Locate platelets.
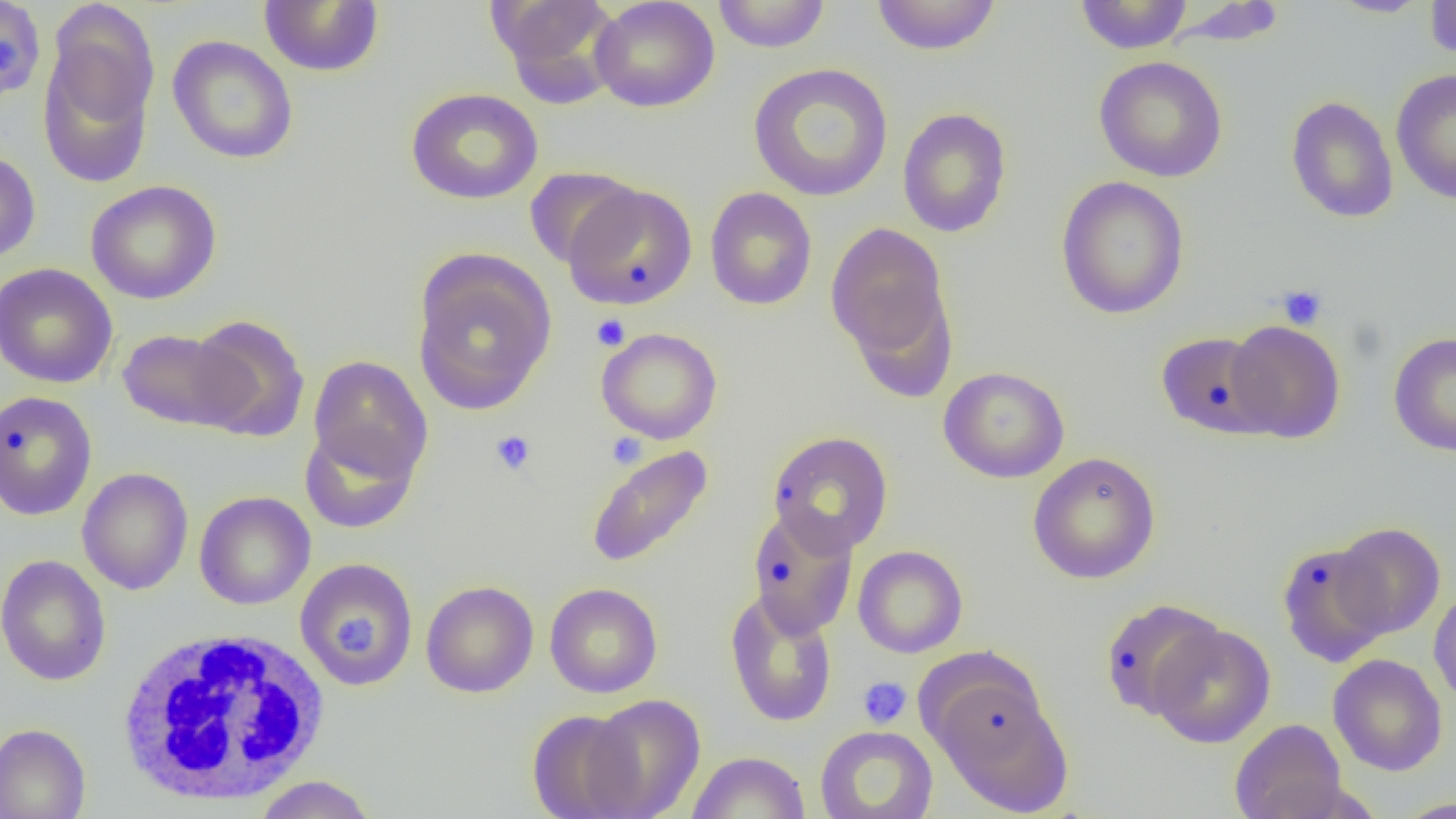

Approximate bounding boxes as named x1/y1/x2/y2 corners in pixels.
Platelets: (x1=1276, y1=284, x2=1328, y2=329), (x1=591, y1=313, x2=631, y2=350), (x1=490, y1=430, x2=536, y2=476), (x1=606, y1=433, x2=647, y2=469), (x1=858, y1=676, x2=912, y2=729).

Summary:
  - White blood cell locations: (x1=114, y1=627, x2=332, y2=807)
  - Uninfected red blood cell locations: (x1=0, y1=0, x2=46, y2=102), (x1=488, y1=0, x2=622, y2=105), (x1=590, y1=0, x2=720, y2=113), (x1=711, y1=0, x2=832, y2=53), (x1=869, y1=0, x2=1002, y2=56), (x1=1073, y1=0, x2=1194, y2=54), (x1=1327, y1=0, x2=1433, y2=18), (x1=1424, y1=0, x2=1456, y2=64), (x1=258, y1=1, x2=385, y2=77), (x1=1166, y1=2, x2=1289, y2=48), (x1=39, y1=33, x2=157, y2=189), (x1=167, y1=35, x2=299, y2=165), (x1=1094, y1=56, x2=1228, y2=182), (x1=748, y1=63, x2=893, y2=202), (x1=1390, y1=69, x2=1456, y2=204), (x1=406, y1=87, x2=544, y2=205), (x1=1285, y1=95, x2=1399, y2=223), (x1=897, y1=107, x2=1013, y2=238), (x1=0, y1=150, x2=40, y2=264), (x1=524, y1=166, x2=642, y2=270), (x1=1055, y1=176, x2=1191, y2=319), (x1=85, y1=180, x2=222, y2=304), (x1=562, y1=182, x2=698, y2=309), (x1=704, y1=186, x2=818, y2=311), (x1=826, y1=221, x2=954, y2=374), (x1=412, y1=251, x2=557, y2=415), (x1=0, y1=263, x2=117, y2=389), (x1=186, y1=314, x2=310, y2=442), (x1=1225, y1=319, x2=1346, y2=443), (x1=596, y1=327, x2=723, y2=445), (x1=117, y1=329, x2=249, y2=431), (x1=1155, y1=331, x2=1277, y2=439), (x1=1388, y1=331, x2=1456, y2=457), (x1=308, y1=355, x2=433, y2=484), (x1=938, y1=366, x2=1070, y2=484), (x1=0, y1=390, x2=98, y2=521), (x1=299, y1=424, x2=420, y2=534), (x1=767, y1=430, x2=894, y2=556), (x1=585, y1=445, x2=714, y2=570), (x1=1028, y1=451, x2=1161, y2=584), (x1=77, y1=467, x2=193, y2=596), (x1=194, y1=491, x2=316, y2=610), (x1=747, y1=507, x2=859, y2=638), (x1=1332, y1=521, x2=1445, y2=640), (x1=1276, y1=540, x2=1393, y2=668), (x1=853, y1=545, x2=968, y2=658), (x1=0, y1=554, x2=112, y2=687), (x1=295, y1=558, x2=419, y2=691), (x1=421, y1=580, x2=539, y2=697), (x1=545, y1=582, x2=663, y2=698), (x1=1428, y1=588, x2=1456, y2=709), (x1=724, y1=590, x2=838, y2=728), (x1=1099, y1=598, x2=1225, y2=720), (x1=1148, y1=622, x2=1276, y2=748), (x1=1328, y1=653, x2=1447, y2=776), (x1=927, y1=669, x2=1071, y2=810), (x1=583, y1=693, x2=706, y2=818), (x1=526, y1=709, x2=647, y2=818), (x1=1229, y1=718, x2=1348, y2=819), (x1=0, y1=723, x2=91, y2=819), (x1=815, y1=725, x2=938, y2=819), (x1=687, y1=751, x2=811, y2=818), (x1=253, y1=775, x2=377, y2=819), (x1=1393, y1=795, x2=1456, y2=818)
  - Slide-level diagnosis: negative for blood parasites
  - Preparation: thin blood smear
  - Magnification: 1000x
  - Modality: optical microscopy
  - Image size: 1456×819 pixels
  - Field of view: one of a larger specimen